Assess this cell for malaria.
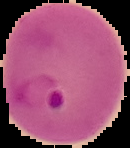

It is parasitized.

{
  "preparation": "thin blood film",
  "image_size": "130×148 pixels",
  "image_type": "cell region segmented out of the field of view; surrounding area masked to black"
}